Draw a bounding box around every malaria parasite.
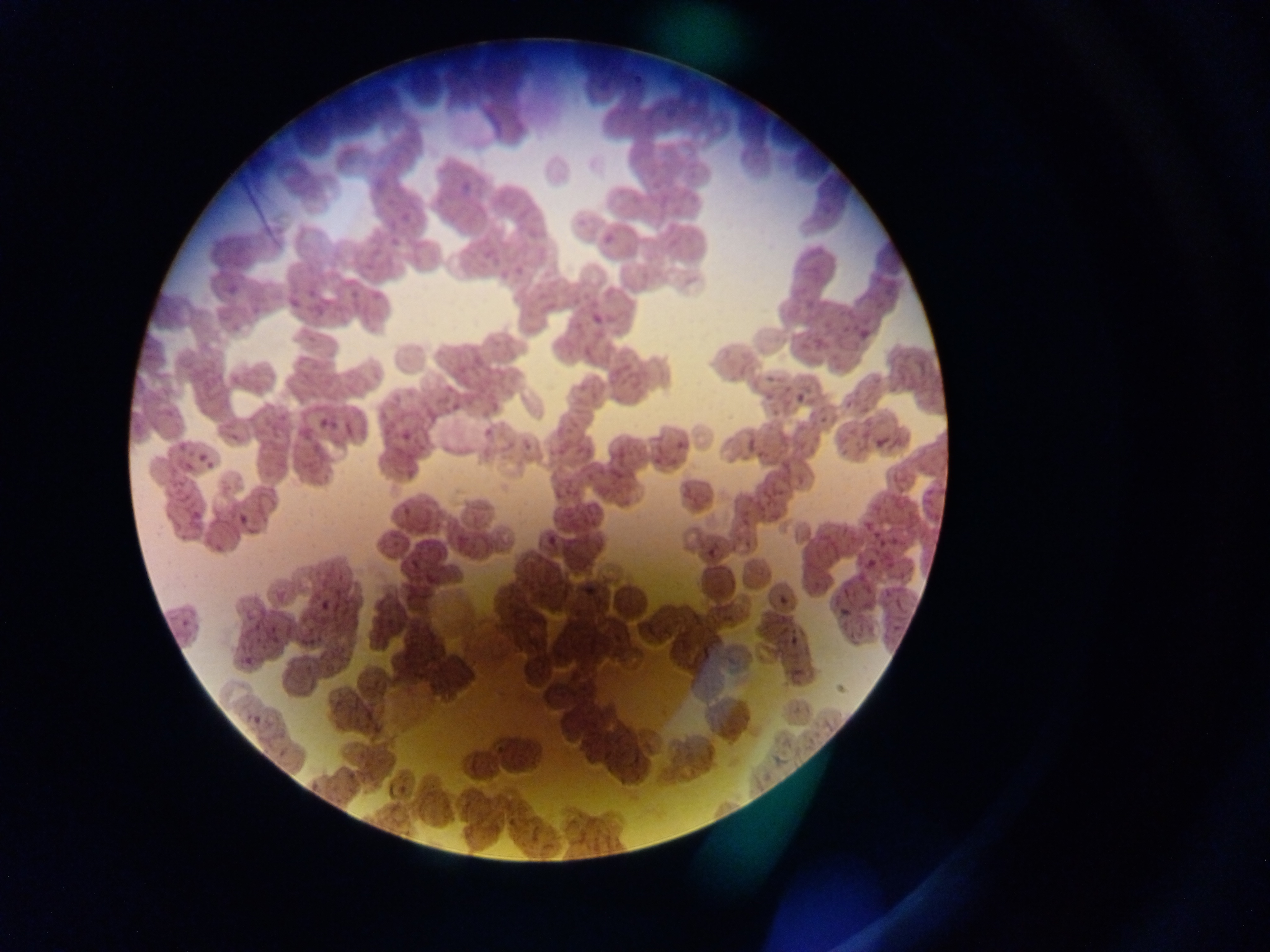
Approximate bounding boxes as (left, top, right, bottom) in pixels.
Malaria parasites: (458, 175, 482, 193), (587, 311, 613, 328), (856, 325, 866, 341), (790, 381, 813, 407), (871, 434, 890, 453), (543, 529, 561, 547), (700, 537, 722, 555), (578, 570, 605, 595), (772, 586, 794, 604), (834, 609, 848, 624), (784, 621, 802, 651), (245, 710, 265, 731).

Image is 1270×952 pixels. Thin blood film. Mobile-phone photograph taken through the microscope. One field of view. Sample from Ghana.